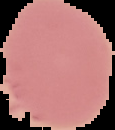
malaria status = uninfected
preparation = thin blood film
image type = segmented cell region on a black background
image size = 115×130 pixels